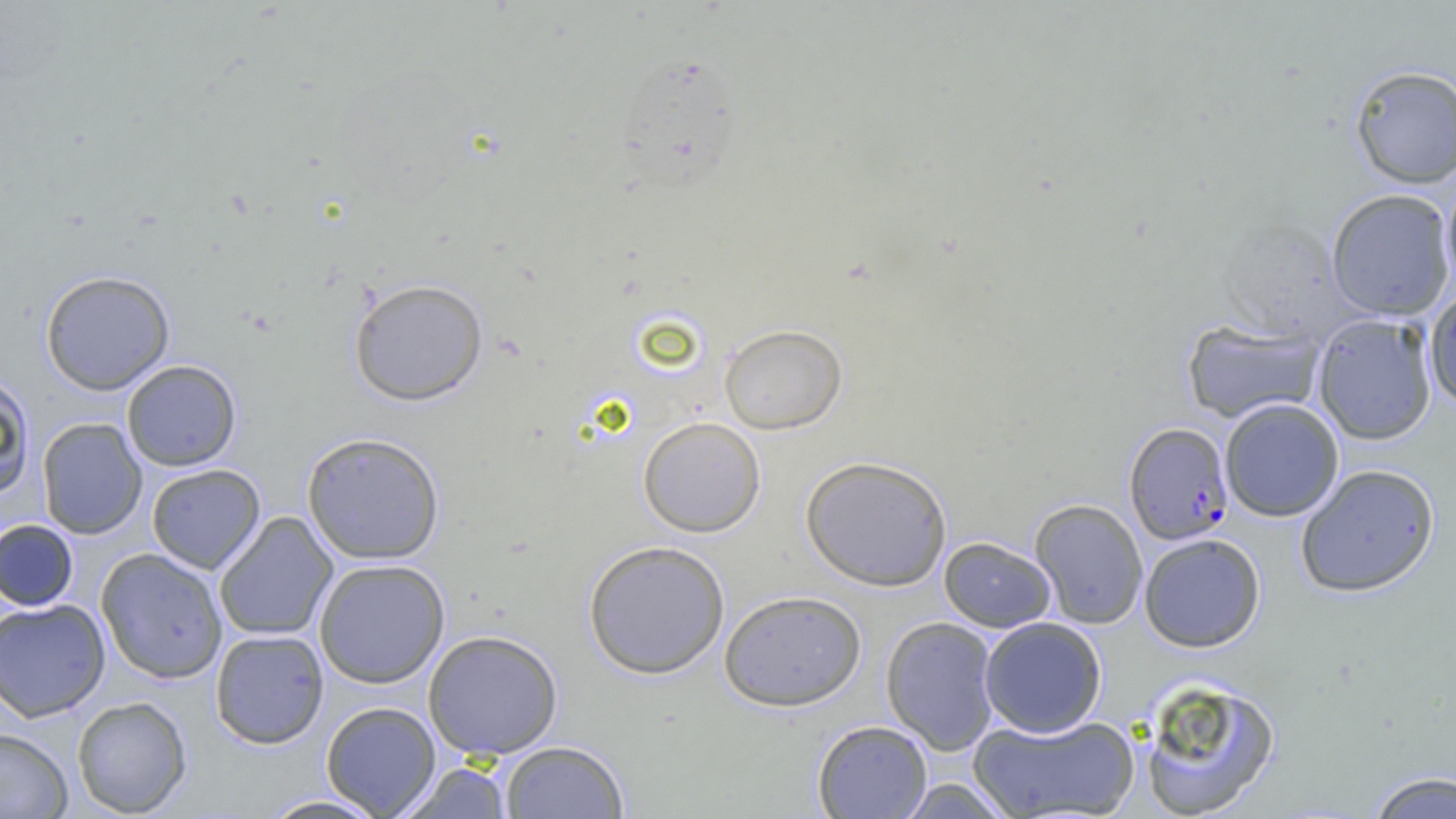

Approximate bounding boxes as [x1, y1, x2, y2] in pixels. Plasmodium falciparum-infected red blood cell locations: [1124, 422, 1234, 545]. Uninfected red blood cell locations: [612, 50, 747, 191], [1349, 64, 1456, 189], [1441, 172, 1456, 294], [1326, 188, 1455, 321], [39, 269, 175, 395], [348, 278, 489, 406], [1424, 289, 1456, 410], [1313, 314, 1437, 445], [1182, 320, 1324, 423], [719, 324, 847, 434], [122, 360, 242, 471], [0, 373, 36, 501], [1219, 398, 1344, 522], [638, 416, 766, 537], [37, 417, 148, 539], [301, 432, 446, 565], [800, 455, 952, 591], [1296, 463, 1440, 597], [146, 464, 265, 574], [1029, 498, 1148, 629], [213, 512, 338, 642], [0, 519, 79, 612], [1139, 533, 1266, 652], [939, 537, 1056, 632], [583, 540, 731, 679], [96, 548, 228, 684], [313, 558, 450, 688], [719, 589, 867, 711], [0, 599, 111, 722], [881, 616, 1000, 756], [979, 616, 1107, 738], [210, 629, 329, 749], [422, 629, 564, 760], [1136, 675, 1282, 819], [72, 696, 192, 817], [321, 701, 441, 817], [967, 714, 1141, 819], [811, 720, 933, 818], [0, 728, 73, 817], [499, 740, 629, 818], [398, 761, 513, 819], [1365, 770, 1455, 819], [896, 778, 1015, 818], [258, 794, 391, 818]. Slide-level diagnosis: Plasmodium falciparum. Image is 1456×819 pixels. Captured at 1000x magnification. Single field of view. Thin blood film. Optical microscopy.